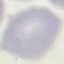

Summary:
  - Malaria status: uninfected
  - Capture: smartphone camera at the microscope eyepiece
  - Stain: Giemsa
  - Preparation: thin blood film
  - Image type: automatically extracted cell patch, resized to 64 × 64 pixels